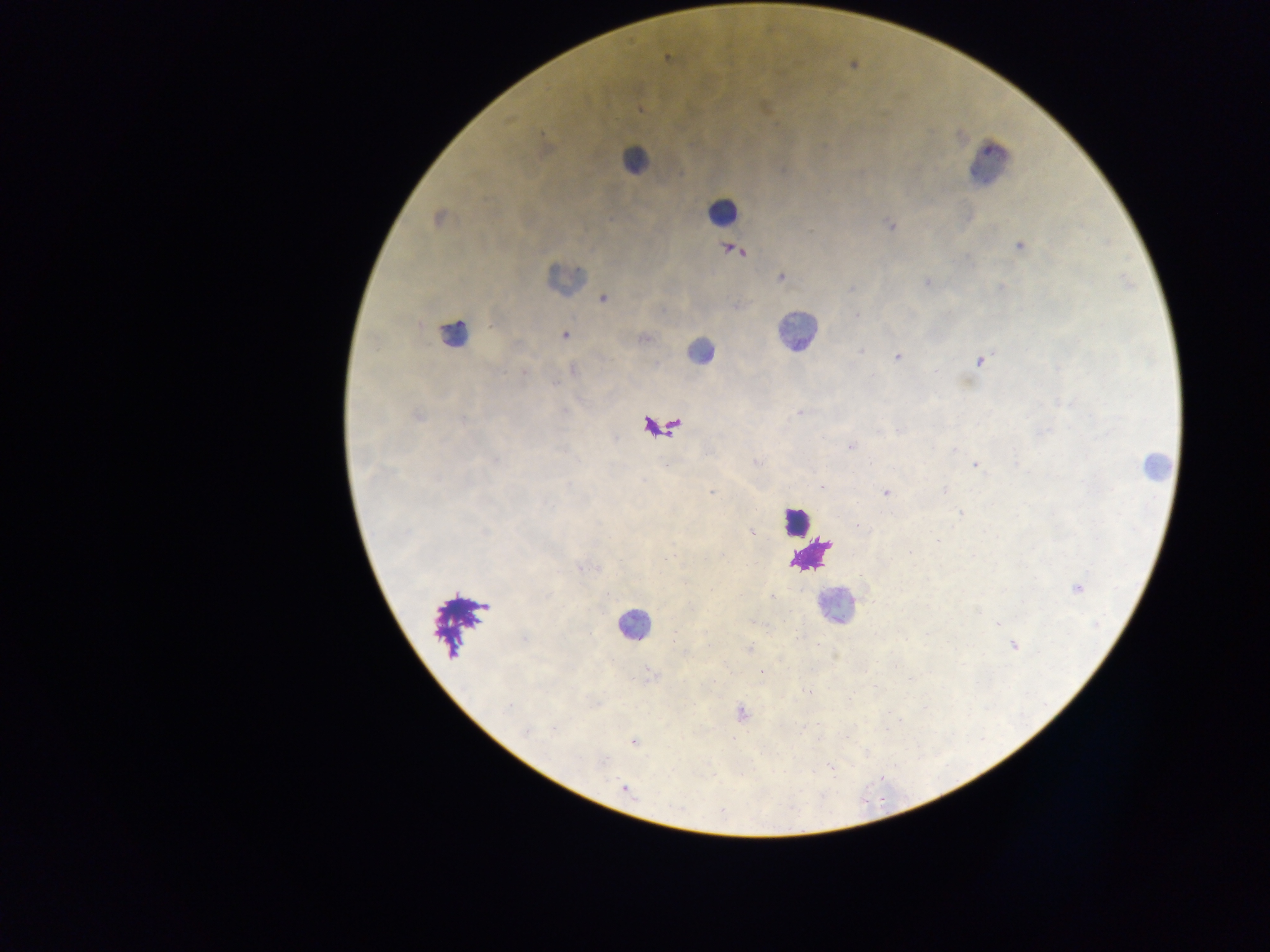
Approximate centers as {x, y} in pixels.
Summary:
  - Malaria parasite locations: {667, 58}, {641, 109}, {680, 173}, {438, 218}, {889, 224}, {1019, 246}, {737, 251}, {781, 277}, {927, 282}, {1001, 287}, {852, 289}, {603, 299}, {857, 315}, {565, 335}, {643, 338}, {860, 351}, {897, 357}, {978, 361}, {573, 370}, {524, 373}, {555, 384}, {799, 413}, {417, 416}, {463, 420}, {901, 430}, {851, 446}, {954, 449}, {757, 462}, {974, 465}, {822, 486}, {945, 491}, {711, 493}, {886, 493}, {960, 513}, {859, 526}, {485, 532}, {752, 532}, {938, 541}, {1077, 588}, {771, 596}, {998, 624}, {524, 638}, {1014, 645}, {750, 648}, {809, 691}, {849, 699}, {507, 706}, {741, 713}, {553, 729}, {525, 731}, {633, 742}, {624, 787}
  - Leukocyte locations: {634, 159}, {989, 163}, {722, 212}, {563, 277}, {796, 331}, {454, 335}, {700, 350}, {1155, 465}, {796, 520}, {833, 606}, {633, 624}
  - Capture: mobile-phone photograph through a microscope
  - Field of view: single
  - Image size: 1270×952 pixels
  - Preparation: thick blood smear
  - Country: Ghana